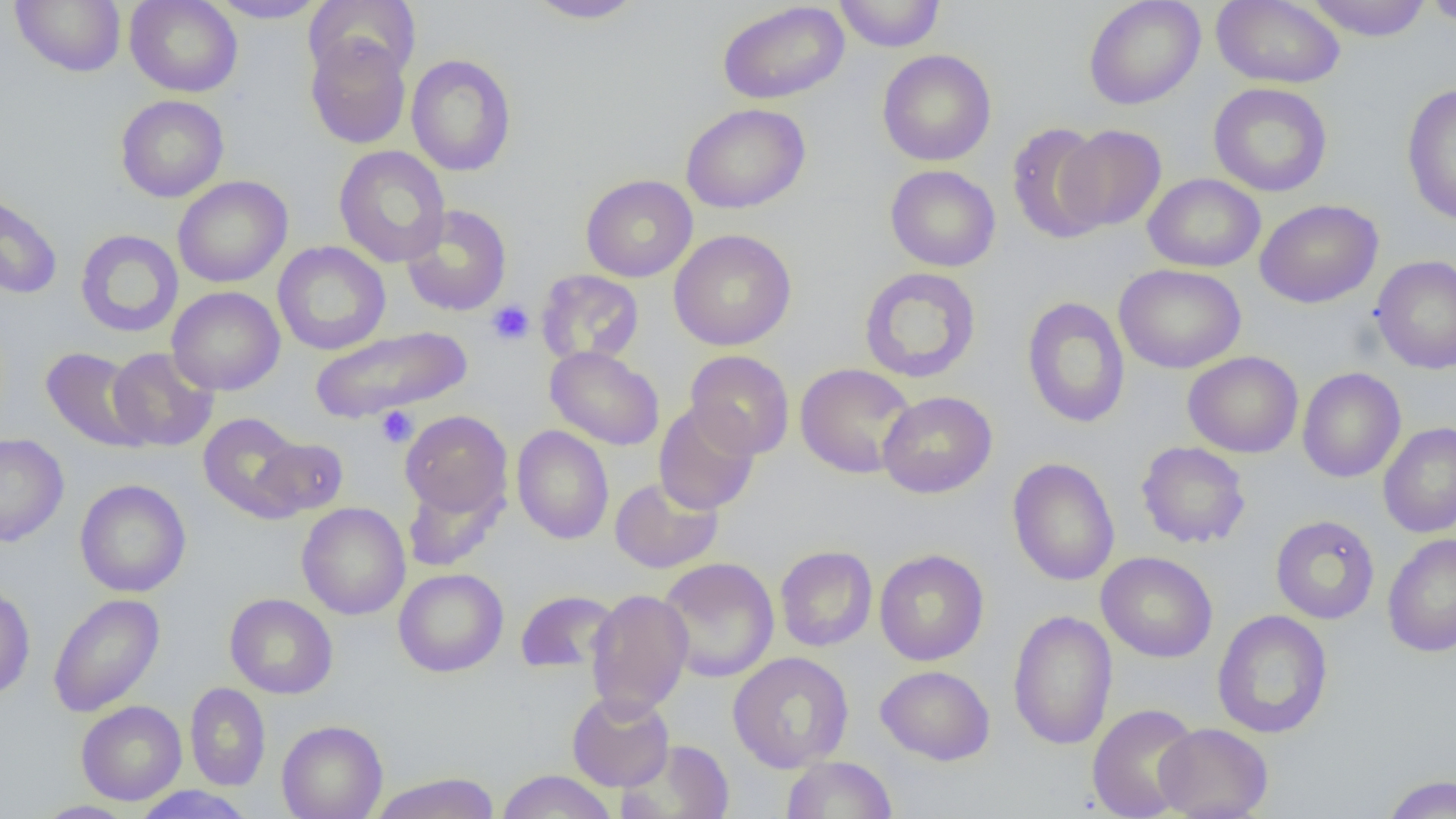
Approximate bounding boxes as named x1/y1/x2/y2 corners in pixels. Uninfected red blood cell locations: (x1=11, y1=0, x2=126, y2=76), (x1=125, y1=0, x2=243, y2=97), (x1=207, y1=0, x2=328, y2=23), (x1=305, y1=0, x2=421, y2=82), (x1=525, y1=0, x2=647, y2=24), (x1=834, y1=0, x2=945, y2=52), (x1=1084, y1=0, x2=1205, y2=110), (x1=1211, y1=0, x2=1345, y2=89), (x1=1303, y1=0, x2=1434, y2=41), (x1=1420, y1=0, x2=1456, y2=27), (x1=717, y1=1, x2=849, y2=104), (x1=305, y1=35, x2=412, y2=149), (x1=306, y1=46, x2=518, y2=159), (x1=877, y1=49, x2=996, y2=166), (x1=405, y1=54, x2=516, y2=176), (x1=1208, y1=83, x2=1332, y2=197), (x1=1401, y1=83, x2=1456, y2=226), (x1=116, y1=95, x2=229, y2=202), (x1=681, y1=103, x2=810, y2=213), (x1=1005, y1=122, x2=1111, y2=244), (x1=1057, y1=124, x2=1167, y2=232), (x1=334, y1=145, x2=450, y2=268), (x1=885, y1=165, x2=1001, y2=272), (x1=1143, y1=173, x2=1266, y2=272), (x1=580, y1=174, x2=698, y2=283), (x1=173, y1=176, x2=292, y2=288), (x1=0, y1=188, x2=63, y2=300), (x1=1255, y1=199, x2=1383, y2=308), (x1=402, y1=205, x2=512, y2=316), (x1=75, y1=229, x2=184, y2=338), (x1=668, y1=229, x2=797, y2=351), (x1=272, y1=241, x2=391, y2=355), (x1=1371, y1=254, x2=1456, y2=374), (x1=1114, y1=264, x2=1246, y2=374), (x1=858, y1=266, x2=982, y2=384), (x1=536, y1=270, x2=644, y2=367), (x1=167, y1=286, x2=284, y2=396), (x1=1021, y1=296, x2=1131, y2=429), (x1=309, y1=325, x2=471, y2=423), (x1=544, y1=346, x2=664, y2=451), (x1=41, y1=347, x2=151, y2=453), (x1=106, y1=347, x2=219, y2=452), (x1=685, y1=350, x2=794, y2=460), (x1=1182, y1=351, x2=1304, y2=458), (x1=795, y1=363, x2=917, y2=479), (x1=1297, y1=367, x2=1406, y2=483), (x1=878, y1=391, x2=997, y2=498), (x1=653, y1=402, x2=760, y2=515), (x1=400, y1=410, x2=512, y2=518), (x1=198, y1=413, x2=307, y2=521), (x1=1378, y1=422, x2=1456, y2=538), (x1=512, y1=425, x2=614, y2=544), (x1=0, y1=433, x2=69, y2=546), (x1=251, y1=436, x2=349, y2=518), (x1=1136, y1=441, x2=1251, y2=549), (x1=1007, y1=457, x2=1120, y2=586), (x1=402, y1=476, x2=506, y2=572), (x1=609, y1=476, x2=723, y2=574), (x1=74, y1=479, x2=191, y2=597), (x1=296, y1=502, x2=411, y2=620), (x1=1270, y1=514, x2=1380, y2=624), (x1=1383, y1=533, x2=1456, y2=657), (x1=775, y1=545, x2=878, y2=651), (x1=874, y1=549, x2=989, y2=666), (x1=1096, y1=551, x2=1218, y2=662), (x1=657, y1=557, x2=779, y2=683), (x1=393, y1=568, x2=509, y2=677), (x1=0, y1=584, x2=35, y2=700), (x1=586, y1=588, x2=693, y2=717), (x1=515, y1=590, x2=620, y2=675), (x1=48, y1=593, x2=165, y2=717), (x1=225, y1=593, x2=338, y2=699), (x1=1212, y1=609, x2=1333, y2=739), (x1=1007, y1=610, x2=1118, y2=750), (x1=728, y1=651, x2=854, y2=773), (x1=876, y1=665, x2=995, y2=765), (x1=185, y1=682, x2=271, y2=791), (x1=567, y1=690, x2=674, y2=791), (x1=76, y1=700, x2=187, y2=805), (x1=1086, y1=703, x2=1201, y2=819), (x1=276, y1=720, x2=388, y2=819), (x1=1154, y1=723, x2=1273, y2=819), (x1=619, y1=740, x2=735, y2=819), (x1=781, y1=755, x2=897, y2=818), (x1=496, y1=770, x2=617, y2=819), (x1=369, y1=772, x2=501, y2=819), (x1=1381, y1=774, x2=1456, y2=818), (x1=131, y1=786, x2=256, y2=819), (x1=33, y1=800, x2=137, y2=819). Platelet locations: (x1=486, y1=300, x2=534, y2=345), (x1=375, y1=405, x2=418, y2=447). Slide-level diagnosis: no evidence of blood parasites. Image is 1456×819 pixels. 1000x magnification. One field of a larger specimen. Optical microscopy. Thin blood film.